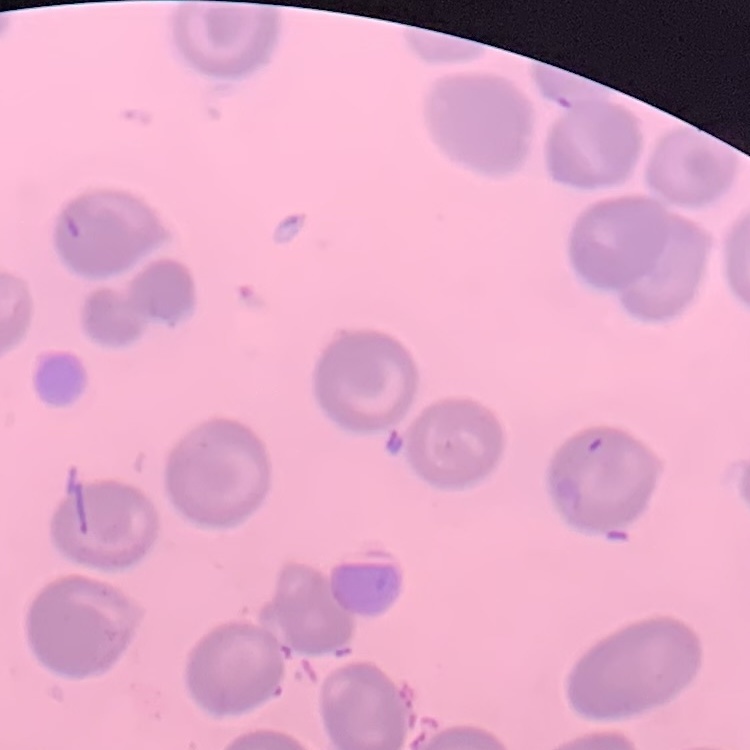

Summary:
  - Erythrocyte morphology: no rouleaux formation
  - Preparation: thin blood smear
  - Image type: one tile cut from a larger photomicrograph
  - Stain: Field's or Giemsa